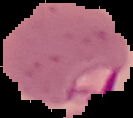

Summary:
  - Malaria status: parasitized
  - Image size: 133×118 pixels
  - Preparation: thin blood smear
  - Image type: segmented cell region with the area outside set to black